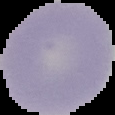
image type = segmented cell region with the area outside set to black
image size = 115×115 pixels
result = no malaria parasites detected
preparation = thin blood film